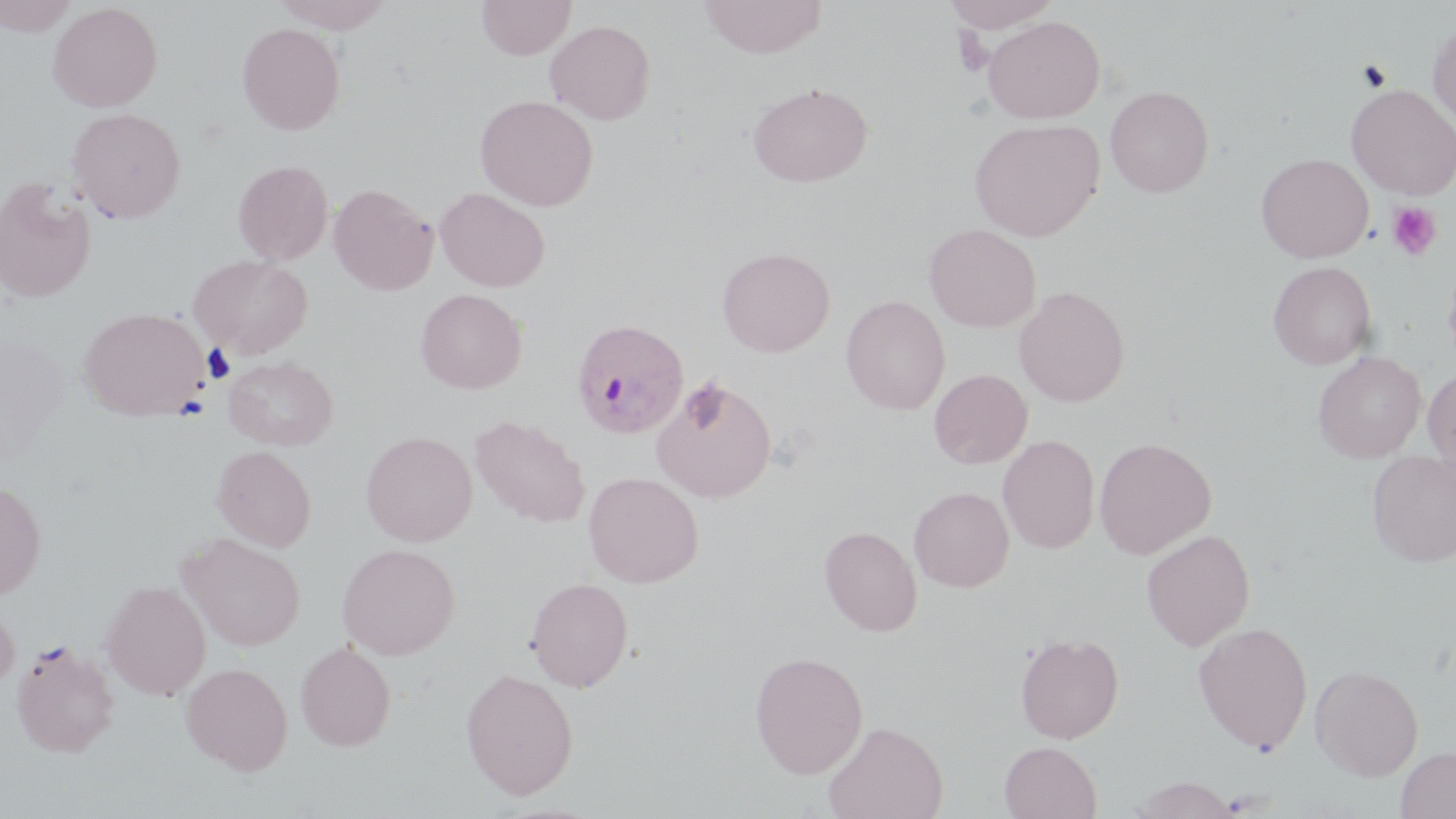
slide-level diagnosis = Plasmodium ovale
magnification = 1000x
preparation = thin blood smear
image size = 1456×819 pixels
stain = May-Grünwald-Giemsa
uninfected red blood cell locations = approximate bounding boxes as [x1, y1, x2, y2] in pixels: [0, 0, 79, 36], [272, 0, 395, 32], [476, 0, 576, 60], [698, 0, 827, 58], [941, 0, 1062, 34], [47, 2, 162, 112], [983, 16, 1105, 123], [544, 19, 655, 125], [237, 22, 345, 135], [1428, 22, 1456, 128], [747, 82, 873, 187], [1346, 84, 1456, 199], [1104, 85, 1214, 197], [475, 95, 598, 211], [66, 108, 186, 223], [969, 118, 1104, 241], [1256, 153, 1374, 262], [232, 160, 334, 265], [0, 177, 97, 302], [328, 183, 437, 295], [435, 187, 550, 292], [923, 223, 1042, 332], [717, 246, 835, 357], [188, 254, 313, 358], [1442, 258, 1456, 370], [1267, 261, 1377, 369], [1013, 286, 1130, 406], [414, 288, 527, 394], [841, 295, 950, 414], [79, 307, 210, 420], [1313, 351, 1426, 463], [223, 356, 338, 450], [1423, 367, 1456, 475], [929, 369, 1032, 469], [651, 377, 777, 503], [469, 414, 590, 528], [360, 431, 477, 546], [998, 435, 1099, 553], [1094, 437, 1216, 559], [212, 445, 316, 551], [1368, 452, 1456, 567], [583, 471, 704, 588], [0, 479, 45, 599], [908, 486, 1014, 592], [819, 525, 922, 637], [1141, 529, 1255, 650], [179, 532, 306, 651], [336, 543, 460, 659], [526, 577, 633, 692], [101, 580, 211, 700], [0, 600, 18, 694], [1193, 621, 1313, 753], [1015, 632, 1124, 744], [11, 640, 119, 757], [295, 642, 395, 751], [749, 651, 869, 778], [181, 662, 293, 775], [1310, 664, 1424, 781], [460, 668, 578, 799], [823, 720, 947, 819], [999, 741, 1102, 819], [1394, 745, 1456, 818], [1128, 775, 1241, 818]
platelet locations = approximate bounding boxes as [x1, y1, x2, y2] in pixels: [1387, 201, 1441, 260]
Plasmodium ovale-infected red blood cell locations = approximate bounding boxes as [x1, y1, x2, y2] in pixels: [571, 318, 689, 439]
modality = light microscopy
field of view = one of a larger specimen